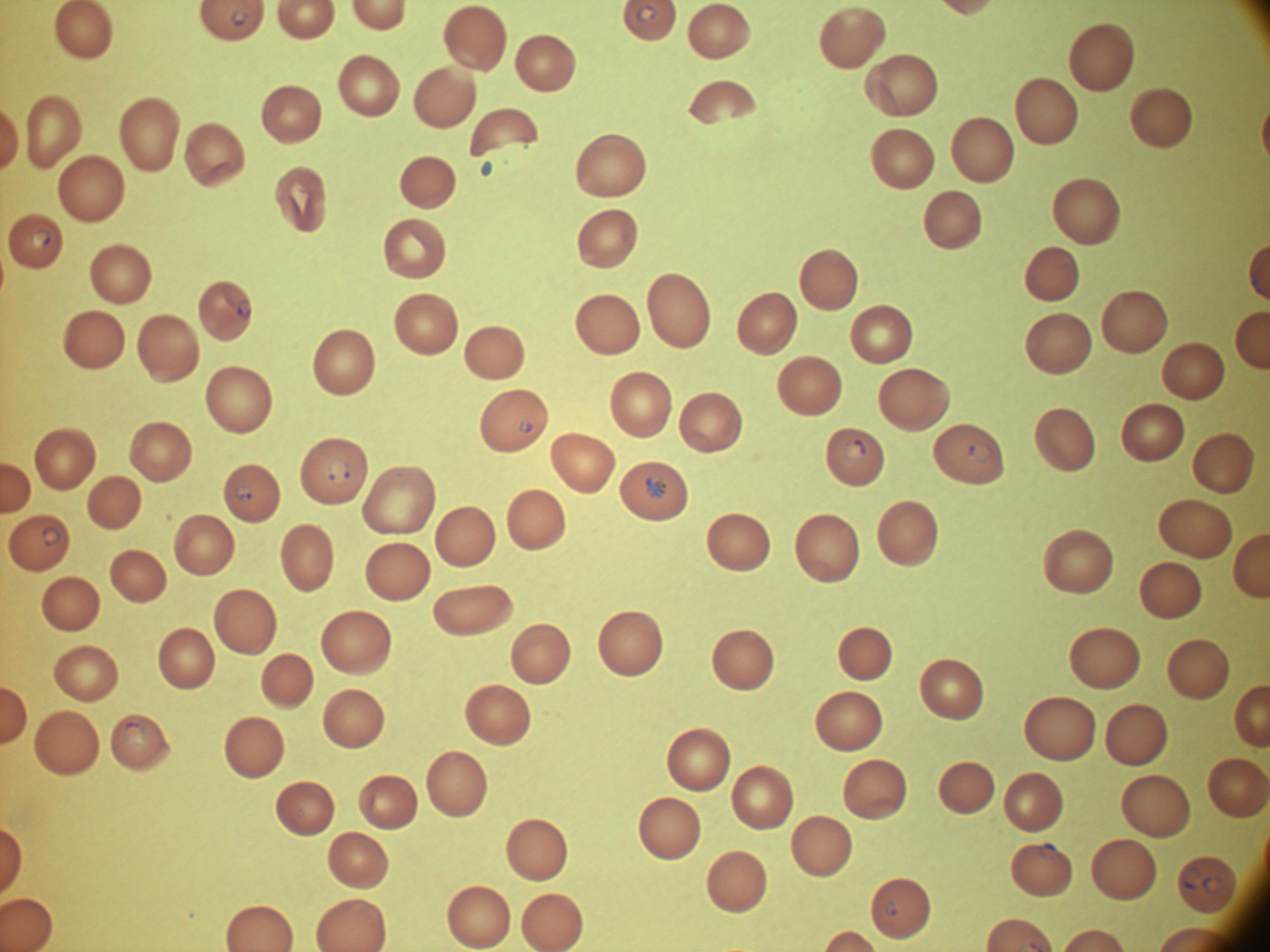

Approximate bounding boxes as named x1/y1/x2/y2 corners in pixels, from the source annotation, which is not necessarily exhaustive.
Summary:
  - Ring form locations: (x1=635, y1=3, x2=659, y2=22), (x1=231, y1=9, x2=249, y2=27), (x1=30, y1=229, x2=51, y2=248), (x1=518, y1=419, x2=534, y2=433), (x1=843, y1=440, x2=868, y2=464), (x1=967, y1=441, x2=994, y2=464), (x1=326, y1=457, x2=350, y2=486), (x1=646, y1=474, x2=668, y2=499), (x1=233, y1=484, x2=253, y2=501), (x1=41, y1=526, x2=61, y2=547), (x1=121, y1=722, x2=146, y2=747), (x1=1038, y1=841, x2=1059, y2=861), (x1=1179, y1=868, x2=1203, y2=889), (x1=1201, y1=876, x2=1223, y2=895), (x1=885, y1=901, x2=898, y2=918)
  - Species: Plasmodium falciparum
  - Field of view: one from this slide
  - Stain: Giemsa
  - Image size: 1270×952 pixels
  - Preparation: thin blood smear
  - Microscope: Leica DM2000 with built-in camera
  - Magnification: 100x